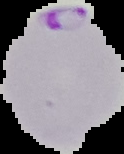

From a thin blood smear. Cell region segmented out of the field of view; the surrounding area is masked to black. Image is 124×154 pixels. Malaria status: parasitized.